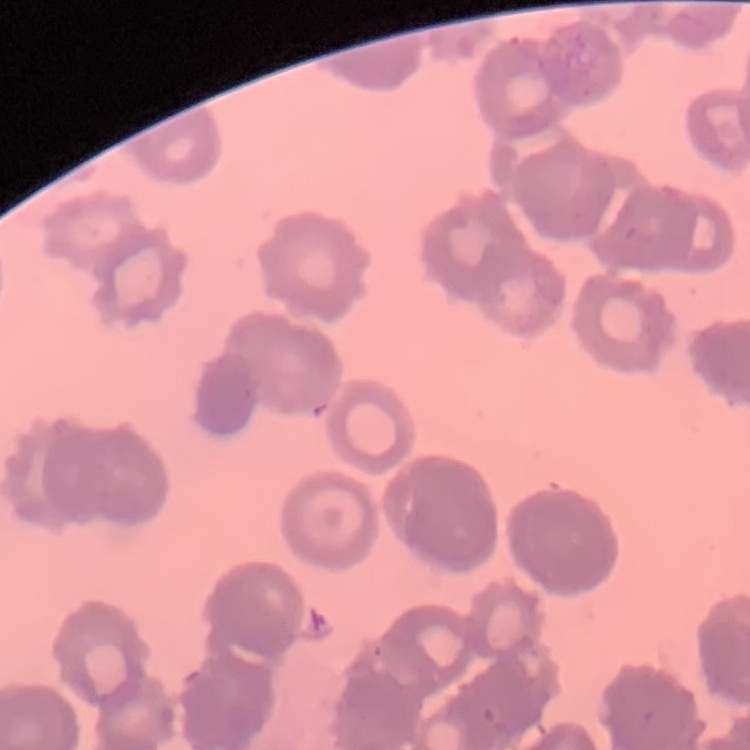
The red blood cells show rouleaux formation. Square crop of a larger photomicrograph. Thin blood film. Stained with either Field's or Giemsa.